Give the position of every Plasmodium parasite, noting whether each is a trophozoite, schizont, or gametocyte.
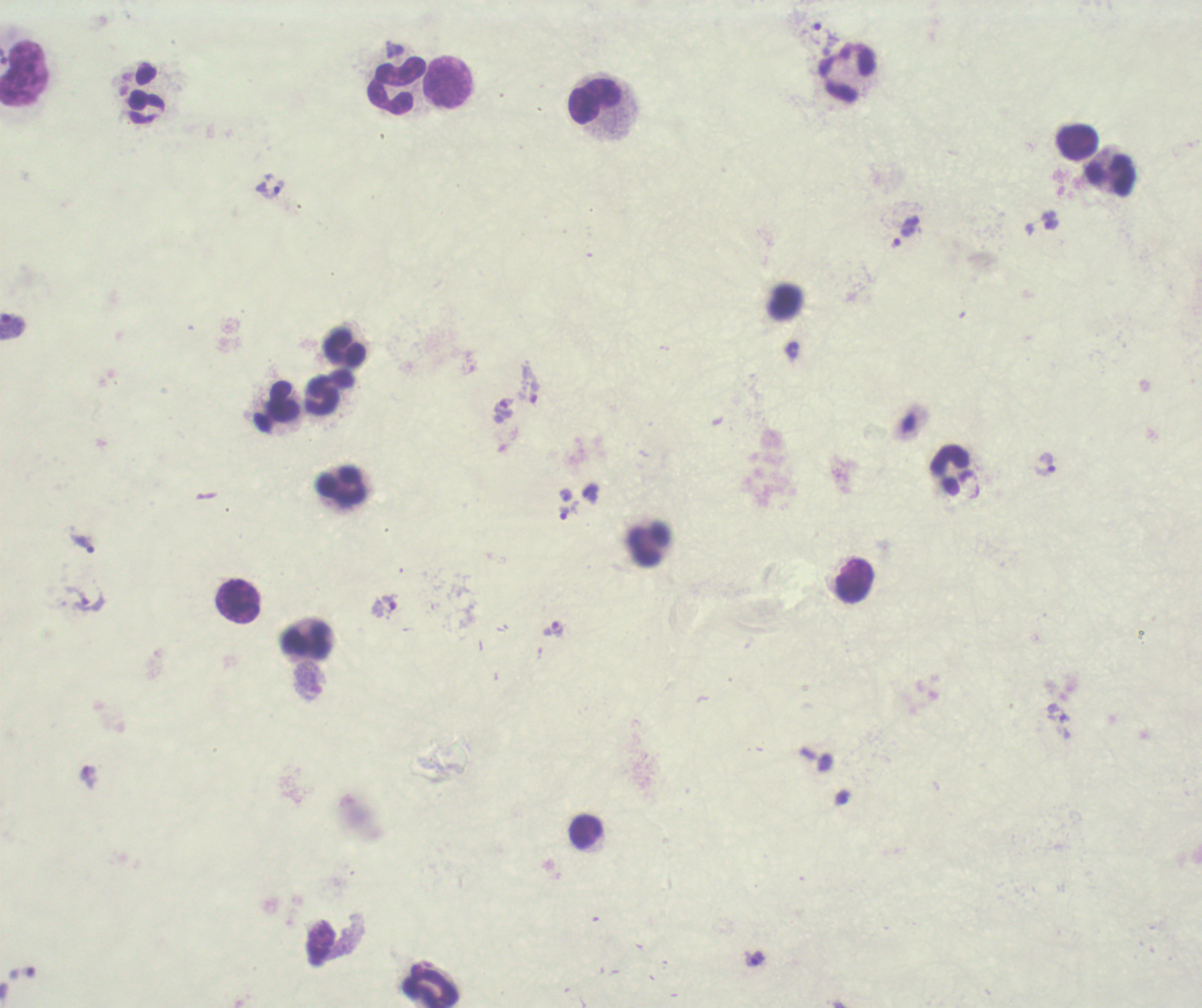

Approximate centers as [x, y] in pixels.
Trophozoites: [823, 33], [395, 49], [270, 189], [906, 231], [12, 326], [530, 391], [1044, 465], [565, 513], [83, 544], [76, 595], [384, 606], [554, 628], [1057, 712], [758, 958].
No schizont or gametocyte forms observed.

Approximate centers as [x, y] in pixels. Leukocyte locations: [846, 72], [24, 73], [448, 82], [395, 87], [147, 93], [595, 100], [1077, 142], [1110, 175], [785, 303], [345, 347], [321, 394], [277, 405], [950, 470], [341, 486], [647, 543], [853, 581], [238, 601], [306, 640], [585, 831], [432, 987]. One field from this slide. Coloration quality: bad. Romanowsky stain. Background quality: unsatisfactory. Image is 1202×1008 pixels. Previously used in a real diagnosis. Captured at 100x magnification. Thick blood smear.